Classify this cell by malaria status.
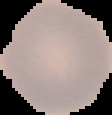
Uninfected.

Summary:
  - Image size: 112×115 pixels
  - Preparation: thin blood smear
  - Image type: segmented cell region on a black background